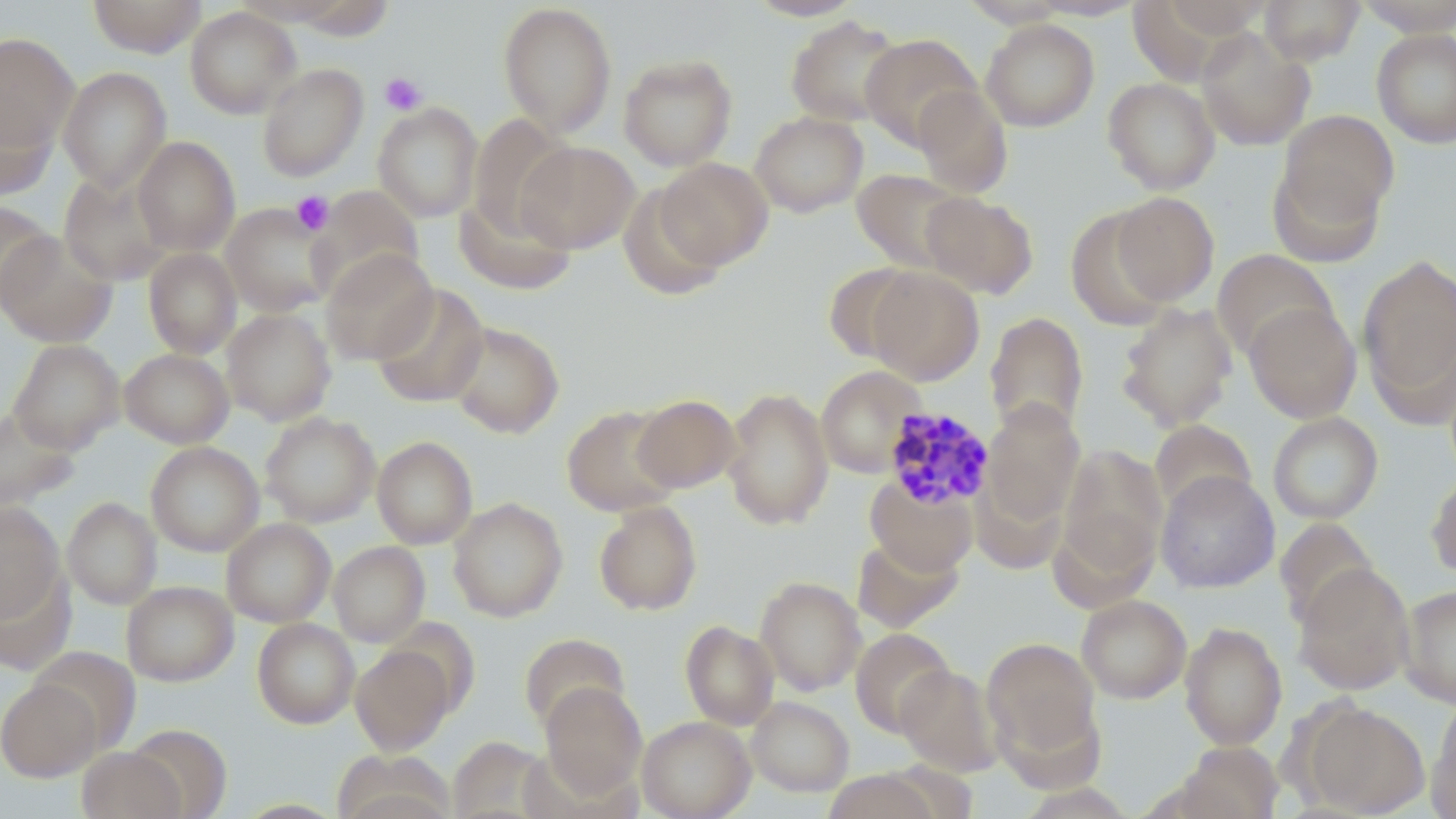

Approximate bounding boxes as (x1, y1, x2, y2) in pixels. Uninfected red blood cell locations: (87, 0, 207, 57), (289, 0, 396, 41), (744, 0, 866, 21), (958, 0, 1073, 27), (1025, 0, 1146, 20), (1141, 0, 1271, 49), (1259, 0, 1365, 66), (1354, 0, 1456, 36), (497, 2, 617, 138), (184, 6, 301, 119), (786, 15, 904, 127), (981, 18, 1099, 132), (1195, 28, 1315, 151), (1371, 29, 1456, 149), (0, 32, 78, 154), (861, 33, 981, 150), (618, 53, 738, 170), (257, 63, 368, 181), (57, 67, 172, 192), (1103, 77, 1220, 194), (912, 85, 1013, 198), (0, 101, 58, 199), (372, 102, 483, 222), (1277, 109, 1399, 228), (750, 111, 868, 217), (468, 114, 575, 235), (132, 136, 240, 256), (516, 141, 639, 253), (656, 157, 772, 268), (1268, 157, 1387, 265), (851, 169, 969, 273), (58, 171, 174, 286), (619, 183, 730, 299), (308, 185, 425, 301), (921, 191, 1038, 299), (454, 192, 577, 295), (1111, 192, 1219, 305), (0, 201, 56, 308), (221, 203, 337, 317), (1066, 207, 1176, 330), (0, 231, 118, 347), (143, 248, 242, 358), (320, 249, 437, 365), (1211, 250, 1339, 361), (1358, 253, 1456, 407), (821, 262, 926, 363), (867, 268, 984, 385), (370, 284, 489, 408), (1116, 302, 1237, 431), (1244, 302, 1361, 423), (221, 307, 336, 425), (985, 312, 1089, 436), (446, 321, 564, 438), (8, 339, 125, 454), (120, 348, 234, 448), (815, 365, 925, 478), (721, 387, 834, 530), (632, 394, 740, 492), (980, 400, 1085, 527), (562, 405, 681, 516), (0, 407, 79, 511), (260, 412, 380, 527), (1267, 412, 1384, 524), (1149, 419, 1257, 516), (372, 436, 477, 549), (146, 441, 264, 556), (1058, 444, 1167, 580), (1155, 470, 1280, 593), (1426, 471, 1456, 579), (866, 478, 978, 575), (62, 497, 162, 609), (447, 498, 567, 622), (593, 500, 702, 615), (0, 502, 66, 623), (1275, 517, 1380, 629), (221, 518, 336, 627), (852, 535, 964, 633), (329, 541, 429, 646), (1293, 563, 1415, 695), (0, 568, 75, 675), (754, 576, 866, 696), (122, 581, 237, 686), (1398, 584, 1456, 707), (1076, 594, 1191, 704), (252, 618, 359, 728), (680, 620, 779, 729), (1180, 622, 1287, 749), (851, 628, 956, 737), (519, 632, 630, 731), (981, 637, 1101, 762), (350, 644, 455, 754), (30, 646, 141, 754), (895, 665, 1004, 775), (0, 679, 101, 781), (540, 683, 647, 796), (746, 696, 854, 796), (1301, 701, 1430, 817), (1428, 701, 1456, 819), (637, 716, 756, 819), (125, 723, 232, 818), (448, 737, 552, 818), (1175, 741, 1284, 819), (77, 747, 184, 819), (333, 749, 456, 817), (820, 769, 941, 819). Plasmodium malariae-infected red blood cell locations: (882, 406, 996, 510). Platelet locations: (379, 72, 428, 116), (291, 191, 334, 234). Slide-level diagnosis: Plasmodium malariae. May-Grünwald-Giemsa-stained preparation. Thin blood film. One field of a larger specimen. Image is 1456×819 pixels. Light microscopy. 1000x magnification.